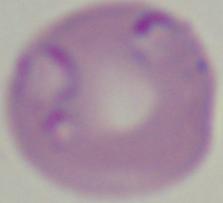
Micrograph. A Babesia parasite is shown. Captured at 1000x magnification.